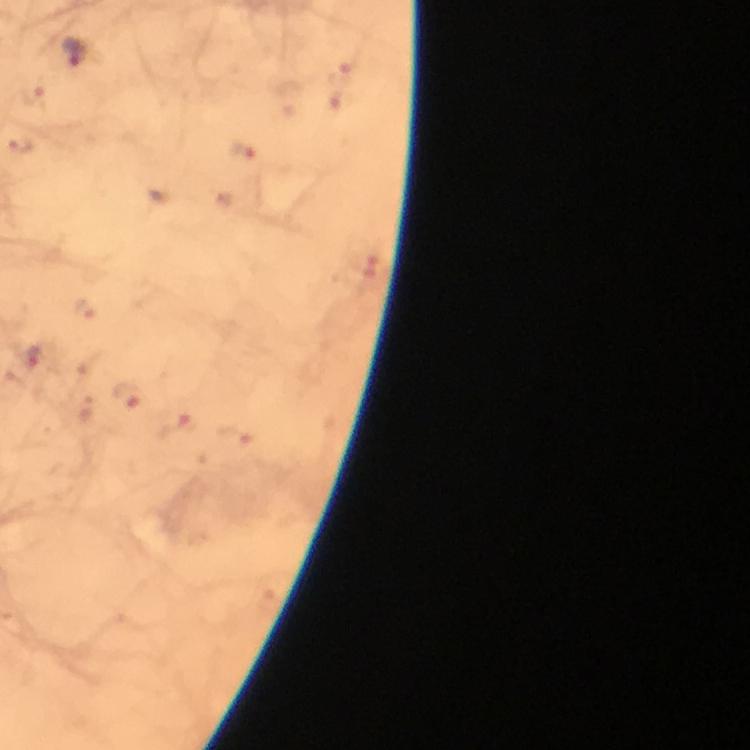
Approximate centers as {x, y} in pixels.
Summary:
  - Malaria parasite locations: {75, 53}, {35, 95}, {25, 144}, {243, 152}, {365, 267}, {84, 307}, {31, 358}, {129, 398}, {177, 422}, {241, 439}
  - Preparation: thick blood smear
  - Stain: Giemsa
  - Immersion oil: applied
  - Image size: 750×750 pixels
  - Cropped from: one field of view
  - Capture: smartphone camera through the microscope
  - Magnification: 100x
  - Context: from a diagnostic examination for malaria